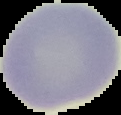

{
  "image_size": "121×115 pixels",
  "malaria_status": "uninfected",
  "preparation": "thin blood smear",
  "image_type": "cell region segmented out of the field of view; surrounding area masked to black"
}